Identify the parasite.
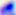

This is Toxoplasma gondii.

Micrograph. 400x magnification.